Identify the preparation type.
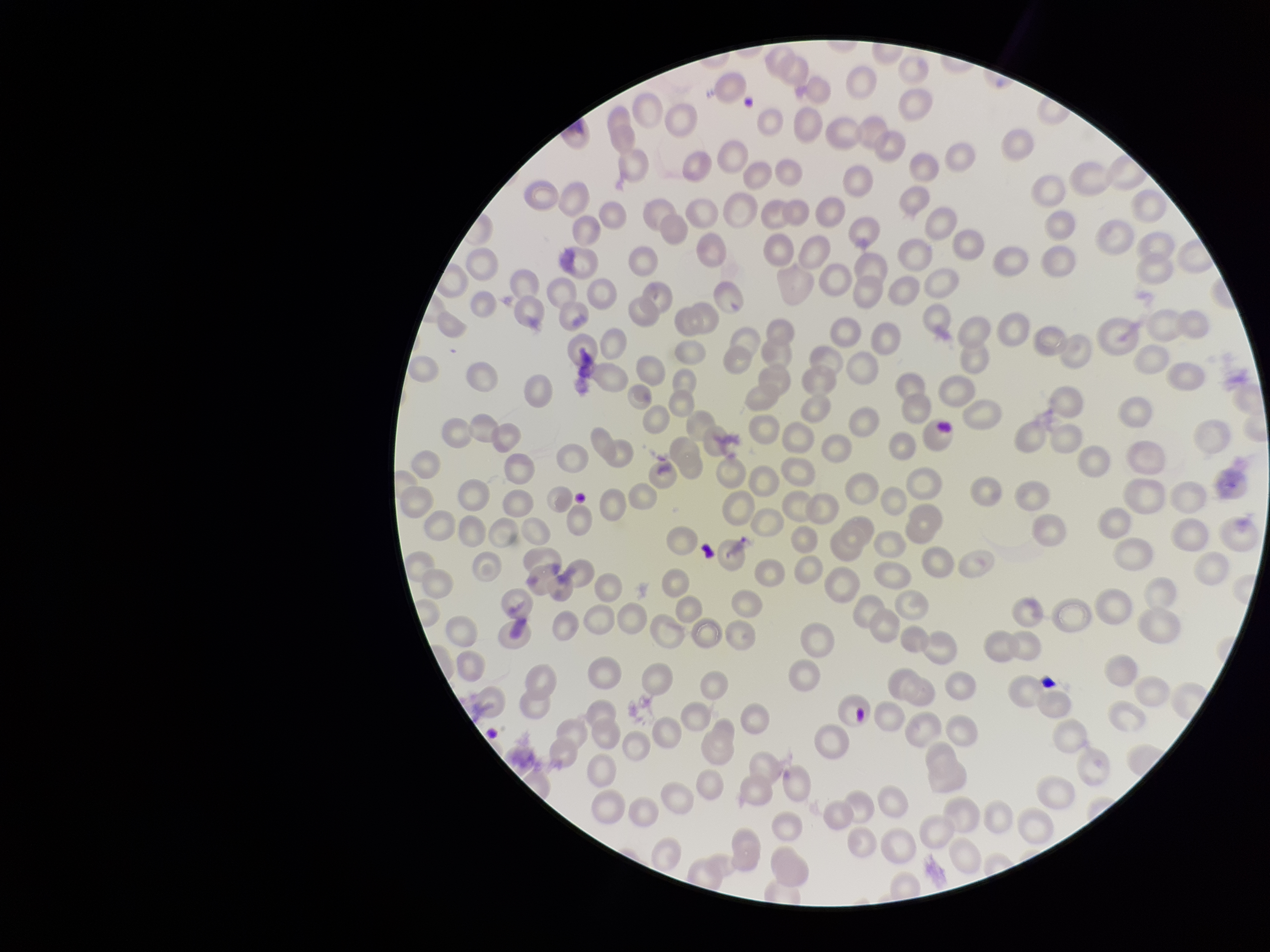

It is a thin blood smear.

Summary:
  - Species reported for this patient: Plasmodium vivax
  - Parasitized red blood cell count: 0
  - Image size: 1270×952 pixels
  - Red blood cell count: 225
  - Patient malaria status: positive
  - Stain: Giemsa
  - Parasitized red blood cells: none identified
  - Capture: smartphone photograph through the microscope eyepiece
  - Field of view: one from this slide